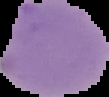
Image is 109×97 pixels. From a thin blood film. Cell region segmented out of the field of view; the surrounding area is masked to black. Result: no Plasmodium parasites seen.